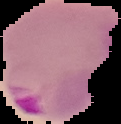

image size = 121×124 pixels
preparation = thin blood film
malaria status = parasitized
image type = cell region segmented out of the field of view; surrounding area masked to black